Outline each Plasmodium falciparum-infected red blood cell.
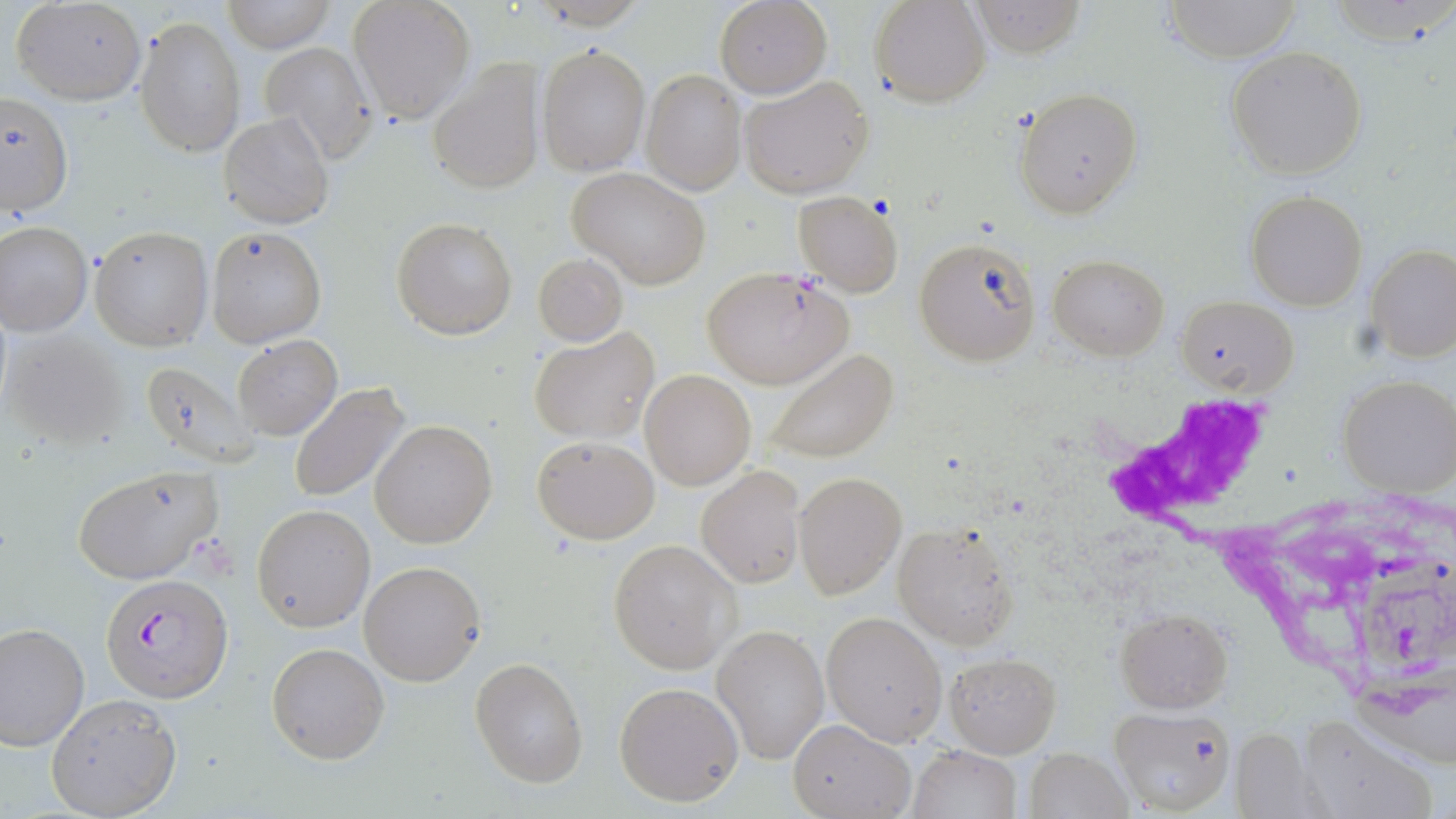

Approximate bounding boxes as [x1, y1, x2, y2] in pixels.
Plasmodium falciparum-infected red blood cells: [704, 267, 853, 389], [102, 574, 230, 702].

Summary:
  - Uninfected red blood cell locations: [12, 0, 147, 106], [218, 0, 336, 52], [347, 0, 475, 123], [870, 0, 992, 107], [714, 1, 832, 98], [970, 1, 1086, 56], [1160, 1, 1305, 63], [136, 18, 245, 156], [256, 40, 377, 164], [538, 44, 649, 176], [1226, 47, 1368, 180], [427, 61, 541, 196], [640, 69, 747, 195], [739, 74, 875, 201], [0, 89, 74, 218], [1015, 90, 1142, 217], [219, 112, 334, 230], [568, 167, 712, 288], [792, 190, 903, 295], [1244, 190, 1367, 311], [391, 216, 518, 339], [0, 220, 94, 335], [88, 225, 214, 351], [206, 228, 326, 346], [913, 235, 1042, 367], [1366, 245, 1456, 363], [1048, 253, 1167, 360], [534, 254, 629, 344], [1177, 294, 1298, 399], [528, 326, 660, 445], [1, 330, 129, 451], [232, 335, 342, 439], [760, 349, 901, 465], [137, 361, 261, 471], [640, 369, 755, 491], [1337, 375, 1455, 496], [288, 383, 412, 503], [368, 420, 496, 549], [532, 433, 659, 544], [696, 465, 806, 588], [71, 466, 224, 586], [792, 471, 904, 599], [252, 504, 377, 633], [894, 520, 1019, 649], [609, 540, 738, 673], [359, 561, 487, 686], [1116, 609, 1233, 711], [820, 611, 947, 745], [0, 623, 90, 752], [713, 623, 829, 765], [267, 642, 389, 764], [946, 652, 1060, 757], [470, 657, 588, 787], [613, 680, 746, 807], [46, 693, 183, 818], [1109, 706, 1234, 816], [1302, 716, 1436, 819], [788, 718, 912, 819], [1231, 728, 1319, 819], [907, 745, 1020, 819], [1025, 747, 1132, 818]
  - White blood cell locations: [1102, 400, 1303, 574]
  - Slide-level diagnosis: Plasmodium falciparum
  - Stain: May-Grünwald-Giemsa
  - Image size: 1456×819 pixels
  - Field of view: single
  - Preparation: thin blood smear
  - Magnification: 1000x
  - Modality: optical microscopy